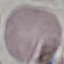

malaria_status: uninfected
capture: smartphone camera at the microscope eyepiece
preparation: thin smear
stain: Giemsa
image_type: cell patch, automatically extracted from a larger field of view and resized to 64 × 64 pixels